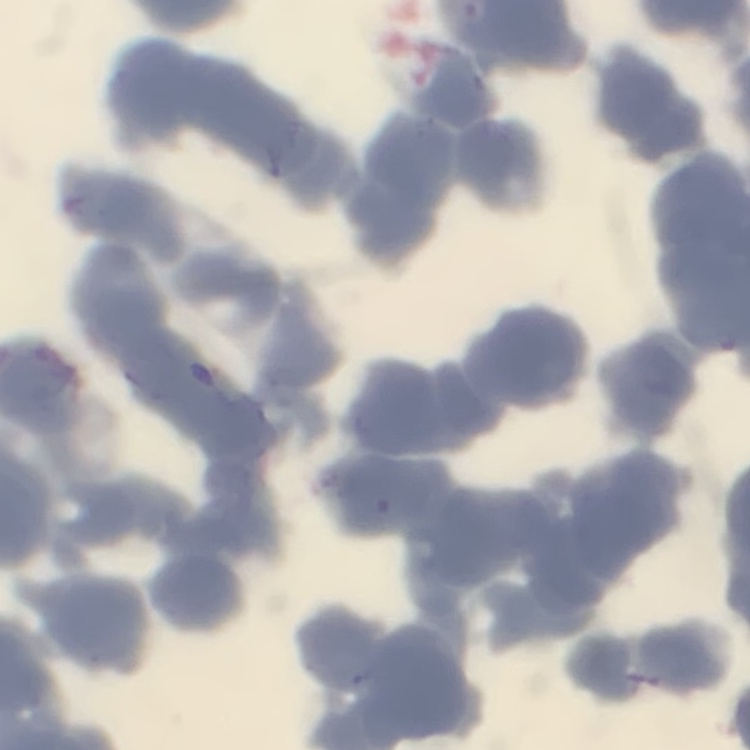

Summary:
  - Erythrocyte morphology: rouleaux formation
  - Image type: one tile cut from a larger photomicrograph
  - Stain: Field's or Giemsa
  - Preparation: thin blood smear